Assess this cell for malaria.
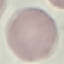

Uninfected.

image type = cell patch, automatically extracted from a larger field of view and resized to 64 × 64 pixels
capture = smartphone camera at the microscope eyepiece
stain = Giemsa
preparation = thin blood smear